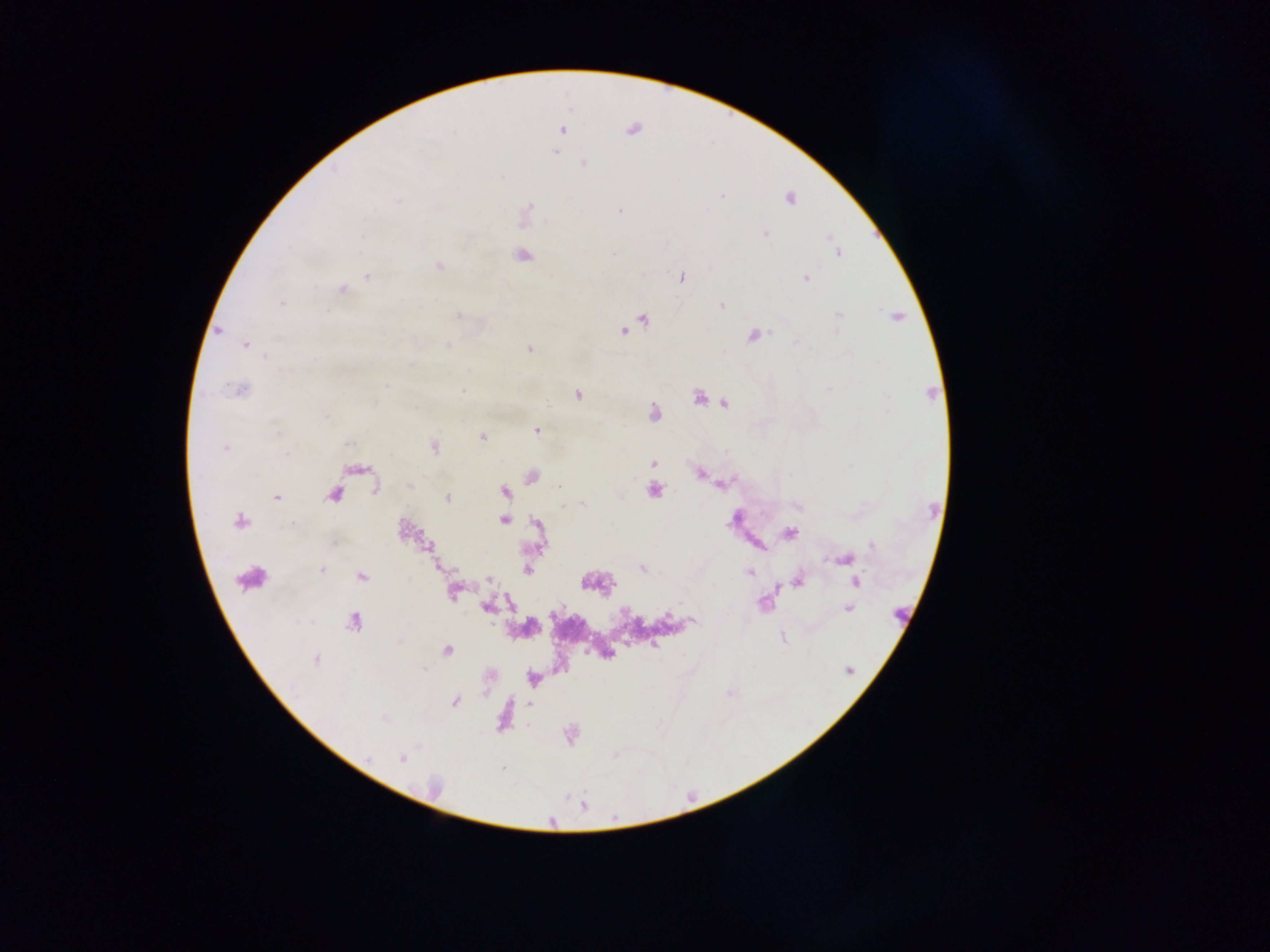

Approximate centers as {x, y} in pixels.
Summary:
  - Malaria parasite locations: {561, 130}, {632, 130}, {455, 133}, {555, 152}, {584, 163}, {721, 196}, {790, 199}, {399, 201}, {619, 210}, {766, 234}, {830, 236}, {838, 254}, {523, 256}, {439, 265}, {367, 277}, {681, 278}, {806, 278}, {342, 289}, {282, 303}, {721, 305}, {838, 315}, {457, 316}, {897, 316}, {644, 320}, {219, 331}, {623, 331}, {753, 335}, {796, 341}, {245, 345}, {447, 347}, {529, 348}, {265, 356}, {386, 386}, {240, 390}, {827, 390}, {461, 391}, {577, 394}, {699, 398}, {725, 403}, {375, 404}, {546, 404}, {652, 413}, {327, 416}, {536, 431}, {481, 437}, {348, 444}, {434, 446}, {225, 448}, {287, 453}, {653, 463}, {700, 475}, {532, 477}, {408, 485}, {558, 487}, {654, 490}, {504, 491}, {334, 494}, {276, 497}, {447, 498}, {583, 505}, {562, 506}, {504, 520}, {239, 521}, {790, 533}, {335, 544}, {872, 546}, {846, 560}, {642, 569}, {320, 570}, {527, 570}, {748, 572}, {361, 577}, {489, 579}, {798, 579}, {856, 582}, {454, 592}, {486, 607}, {848, 608}, {668, 615}, {353, 620}, {693, 620}, {782, 638}, {655, 646}, {447, 651}, {315, 660}, {424, 670}, {849, 670}, {455, 701}, {529, 704}, {384, 718}, {401, 758}
  - Leukocyte locations: {250, 575}
  - Image size: 1270×952 pixels
  - Preparation: thick blood film
  - Field of view: single
  - Capture: mobile-phone photograph through a microscope
  - Country: Ghana